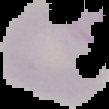

Summary:
  - Image size: 109×109 pixels
  - Result: no Plasmodium parasites seen
  - Preparation: thin blood smear
  - Image type: segmented cell region with the area outside set to black